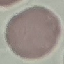
malaria_status: uninfected
stain: Giemsa
capture: smartphone camera at the microscope eyepiece
preparation: thin blood smear
image_type: cell patch, automatically extracted from a larger field of view and resized to 64 × 64 pixels